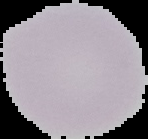

From a thin blood smear. The area outside the segmented cell region is set to black. Malaria status: uninfected. Image is 148×139 pixels.